Comment on the morphology of the erythrocytes.
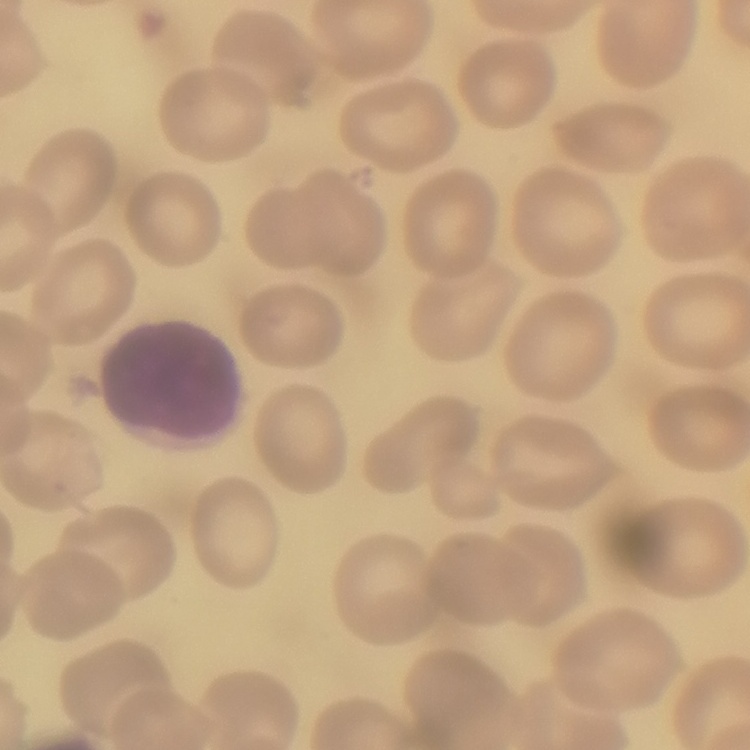
They show no rouleaux formation.

Summary:
  - Preparation: thin peripheral smear
  - Stain: Field's or Giemsa
  - Image type: one tile cut from a larger photomicrograph